Assess this cell for malaria.
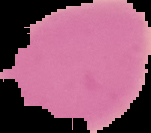
It is uninfected.

image size = 151×133 pixels
preparation = thin blood smear
image type = segmented cell region with the area outside set to black